Outline each Plasmodium malariae-infected red blood cell.
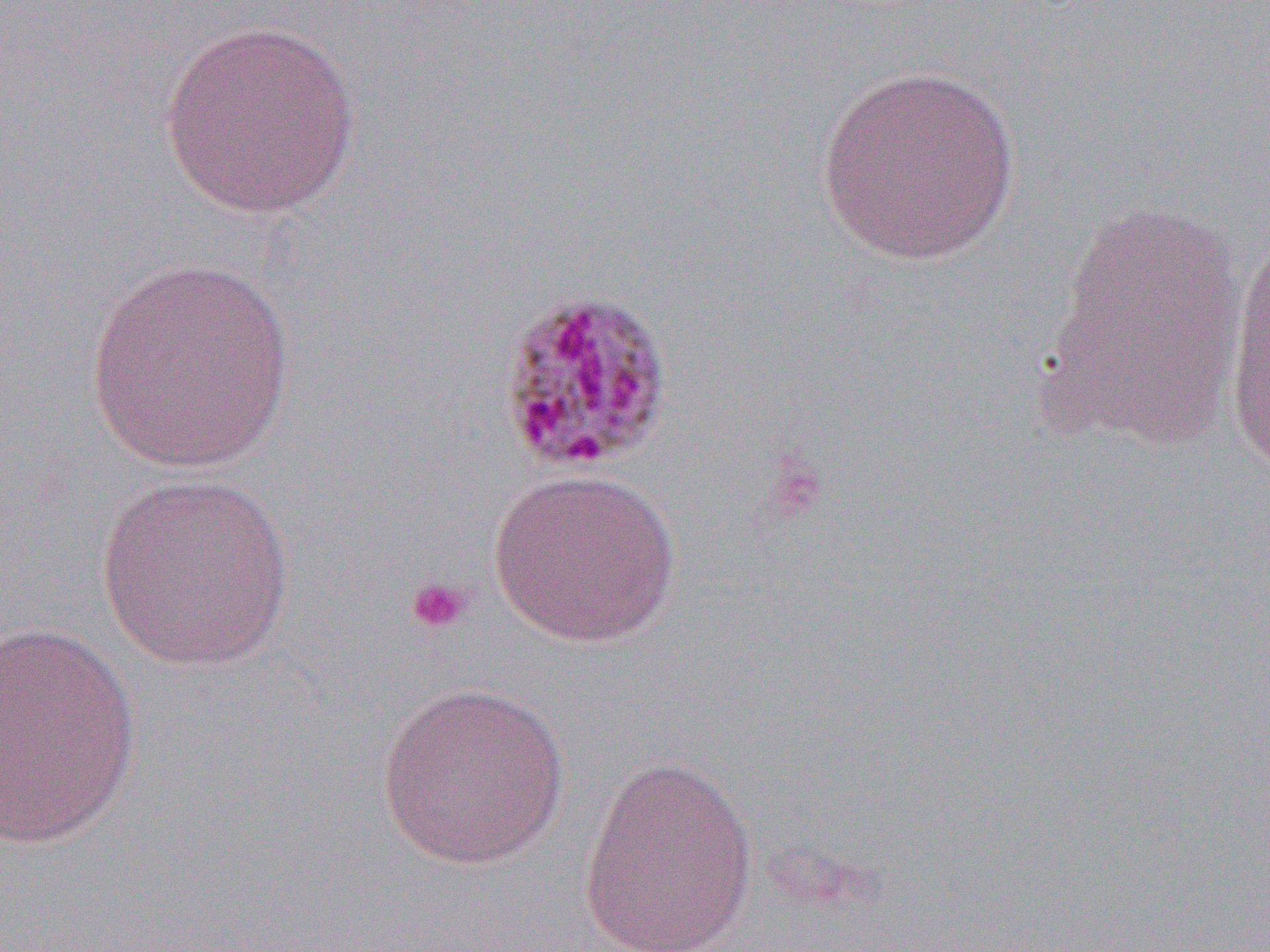

Approximate bounding boxes as (x1,y1)-(x2,y2) corner pairs in pixels.
Plasmodium malariae-infected red blood cells: (494,287)-(676,476).

slide-level diagnosis = Plasmodium malariae
uninfected red blood cell locations = approximate bounding boxes as (x1,y1)-(x2,y2) corner pairs in pixels: (157,19)-(363,220), (816,64)-(1021,266), (1035,198)-(1249,453), (1221,223)-(1269,482), (83,257)-(296,475), (486,467)-(682,648), (94,472)-(297,673), (0,621)-(140,851), (375,679)-(570,870), (578,752)-(759,952)
field of view = single
image size = 1270×952 pixels
magnification = 1000x
modality = optical microscopy
platelet locations = approximate bounding boxes as (x1,y1)-(x2,y2) corner pairs in pixels: (404,575)-(472,634)
preparation = thin blood film